Report the malaria status of this cell.
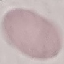
Uninfected.

Summary:
  - Preparation: thin blood smear
  - Image type: automatically extracted cell patch, resized to 64 × 64 pixels
  - Stain: Giemsa
  - Capture: smartphone through the microscope eyepiece